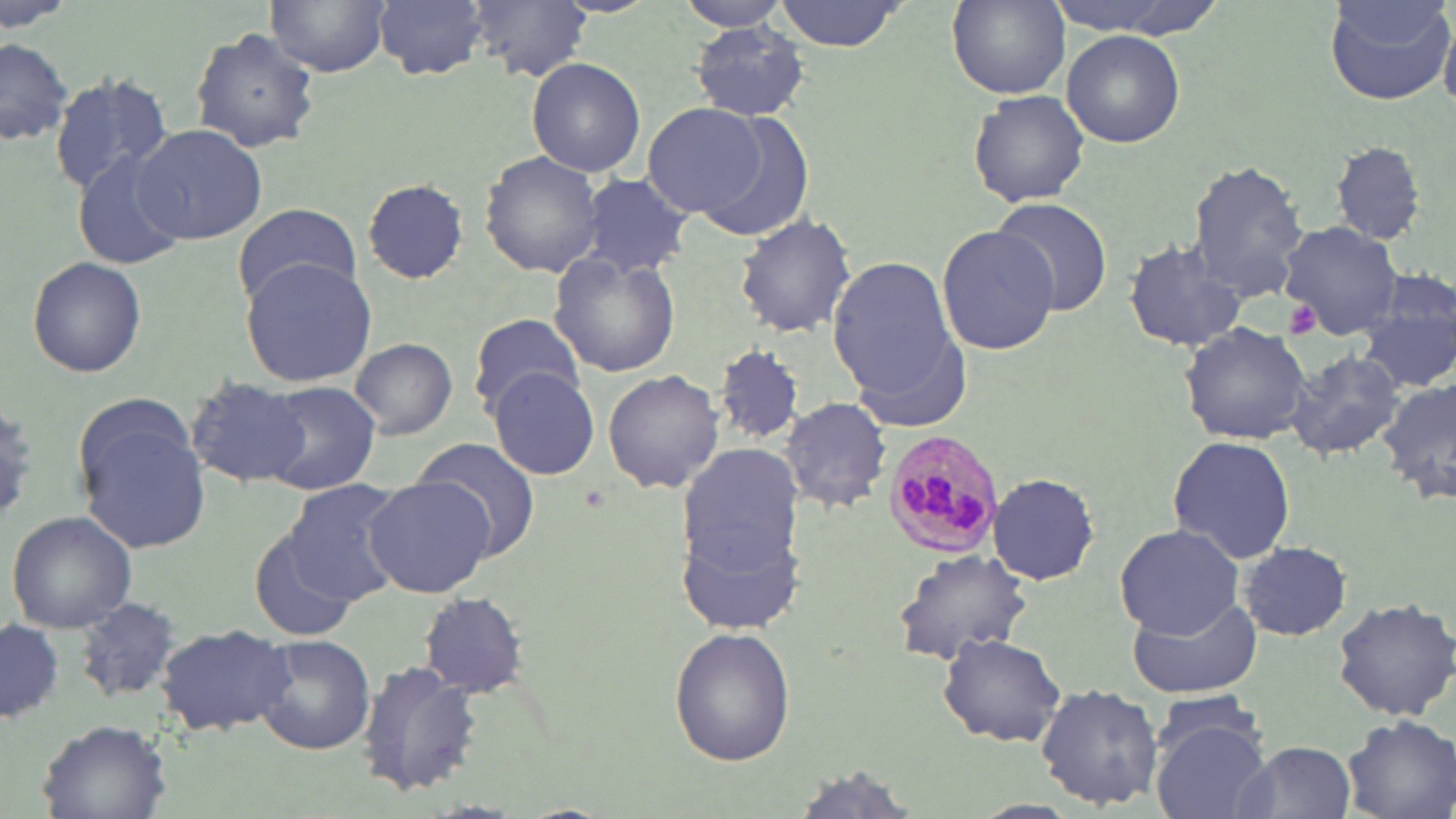

{
  "slide_level_diagnosis": "Plasmodium malariae",
  "preparation": "thin blood film",
  "modality": "optical microscopy",
  "uninfected_red_blood_cell_locations": "approximate bounding boxes as [x1, y1, x2, y2] in pixels: [265, 0, 392, 76], [374, 0, 490, 80], [464, 0, 590, 83], [681, 0, 796, 34], [772, 0, 914, 51], [948, 0, 1070, 97], [1043, 0, 1223, 39], [1325, 0, 1456, 107], [691, 22, 812, 121], [189, 27, 320, 153], [1061, 29, 1185, 148], [0, 34, 75, 151], [1007, 46, 1182, 191], [526, 58, 645, 177], [48, 73, 173, 192], [967, 89, 1091, 208], [643, 102, 768, 218], [697, 114, 813, 242], [133, 124, 267, 246], [1329, 140, 1428, 246], [479, 150, 603, 279], [74, 153, 192, 271], [1186, 157, 1308, 298], [580, 173, 695, 280], [361, 179, 468, 282], [989, 197, 1115, 316], [230, 200, 359, 307], [734, 212, 857, 338], [1281, 220, 1399, 335], [935, 224, 1060, 358], [1126, 236, 1249, 352], [548, 252, 681, 378], [828, 254, 959, 400], [26, 255, 147, 378], [239, 259, 376, 387], [1357, 274, 1456, 394], [467, 311, 584, 417], [1179, 322, 1313, 445], [848, 328, 977, 435], [350, 336, 457, 440], [716, 345, 805, 445], [1280, 350, 1408, 462], [488, 367, 602, 481], [602, 369, 725, 496], [183, 375, 312, 488], [1380, 375, 1456, 509], [256, 382, 380, 495], [73, 394, 210, 549], [781, 396, 892, 513], [1167, 434, 1296, 564], [677, 435, 807, 632], [415, 438, 543, 559], [988, 472, 1100, 587], [362, 474, 500, 598], [281, 480, 406, 603], [6, 509, 137, 633], [1114, 524, 1243, 640], [247, 530, 354, 640], [1239, 543, 1350, 641], [890, 549, 1033, 665], [1128, 589, 1263, 699], [419, 591, 527, 697], [1331, 594, 1456, 720], [75, 598, 184, 702], [2, 618, 63, 730], [155, 622, 295, 738], [669, 627, 797, 767], [252, 634, 376, 757], [937, 634, 1067, 746], [357, 658, 483, 798], [1034, 683, 1165, 810], [1150, 690, 1267, 765], [1147, 714, 1271, 818], [1339, 714, 1455, 819], [35, 722, 171, 817], [1233, 739, 1358, 818]",
  "platelet_locations": "approximate bounding boxes as [x1, y1, x2, y2] in pixels: [1286, 302, 1321, 338]",
  "field_of_view": "single",
  "stain": "May-Grünwald-Giemsa",
  "image_size": "1456×819 pixels",
  "plasmodium_malariae_infected_red_blood_cell_locations": "approximate bounding boxes as [x1, y1, x2, y2] in pixels: [881, 430, 1006, 562]",
  "magnification": "1000x"
}